Classify this cell by malaria status.
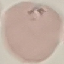
It is uninfected.

Cell patch, automatically extracted from a larger field of view and resized to 64 × 64 pixels. Thin blood smear. Photographed with a smartphone camera at the microscope eyepiece. Giemsa-stained preparation.